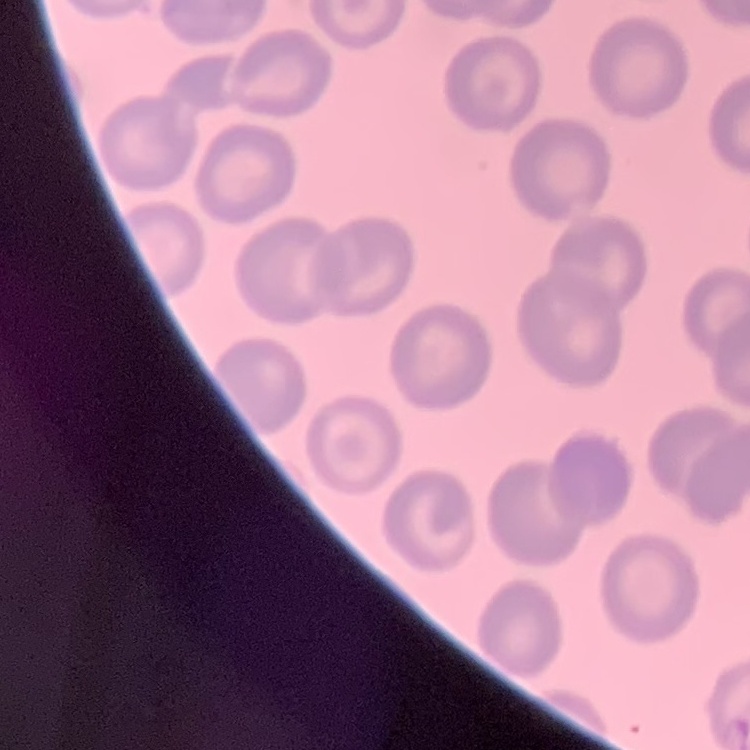 The erythrocytes exhibit no rouleaux formation. Thin peripheral smear. Stained with either Field's or Giemsa. One tile cut from a larger photomicrograph.